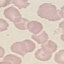
Summary:
  - Result: no malaria parasites seen
  - Image type: automatically extracted cell patch, resized to 64 × 64 pixels
  - Capture: smartphone camera at the microscope eyepiece
  - Stain: Giemsa
  - Preparation: thin blood smear